State which parasite is depicted.
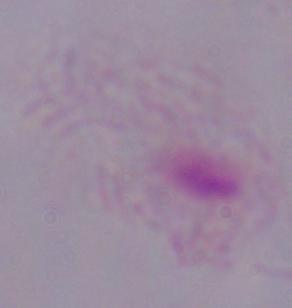
A trichomonad.

Summary:
  - Modality: micrograph
  - Magnification: 1000x